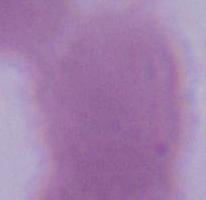
modality = photomicrograph
magnification = 1000x
identification = red blood cell